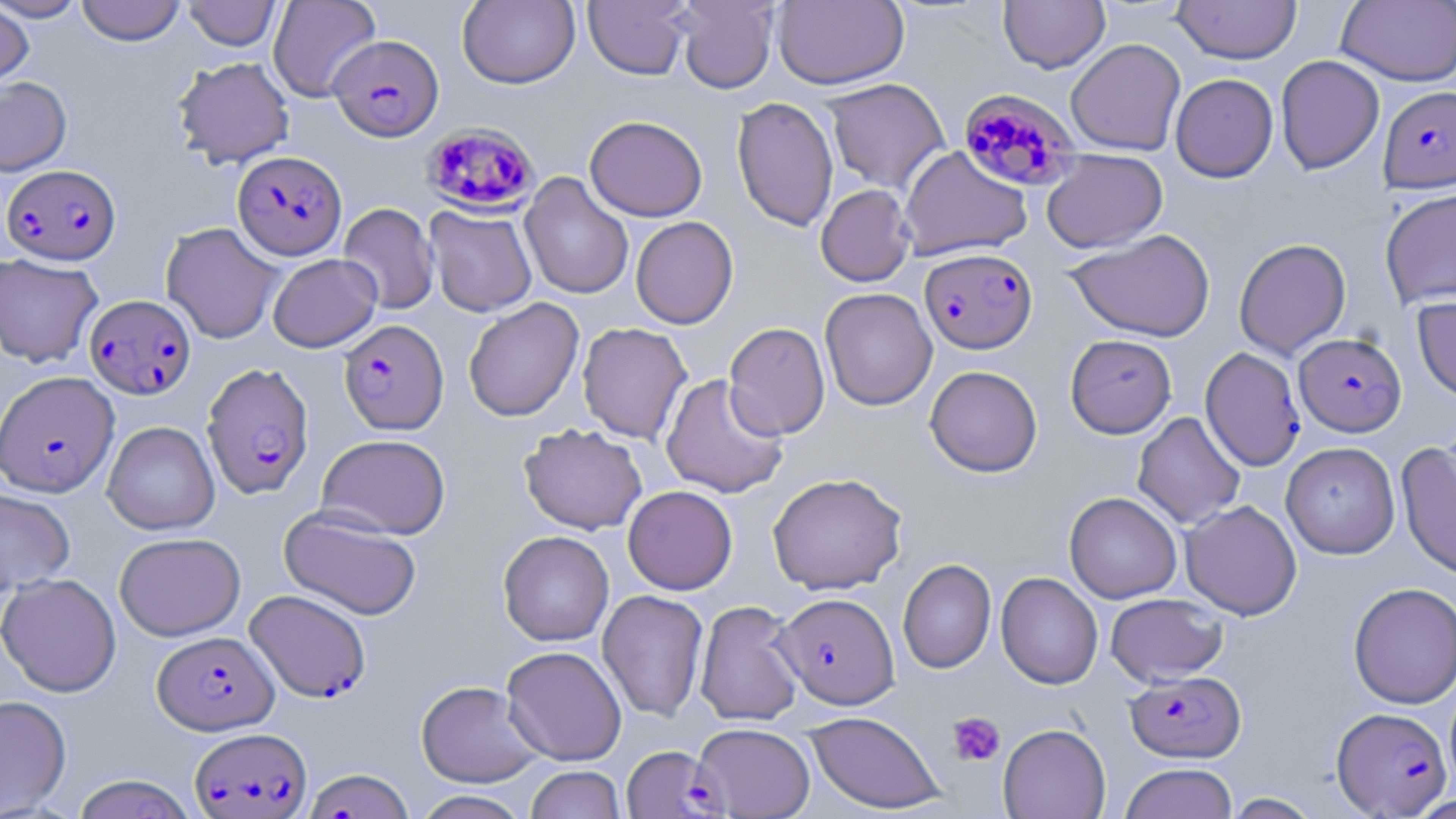

Approximate bounding boxes as [x1, y1, x2, y2] in pixels. Uninfected red blood cell locations (subset): [0, 0, 88, 21], [268, 0, 381, 101], [457, 0, 580, 89], [583, 0, 692, 80], [673, 0, 779, 94], [773, 0, 909, 89], [1337, 0, 1456, 87], [75, 1, 186, 46], [183, 1, 282, 50], [998, 1, 1110, 73], [1172, 1, 1302, 64], [0, 3, 34, 92], [1065, 38, 1186, 156], [1276, 55, 1384, 174], [171, 56, 295, 168], [1170, 73, 1279, 182], [0, 76, 72, 176], [822, 78, 950, 194], [732, 96, 839, 231], [585, 115, 708, 221], [899, 145, 1032, 261], [1041, 149, 1168, 253], [519, 172, 634, 300], [816, 185, 915, 286], [1379, 188, 1456, 309], [338, 203, 439, 315], [425, 206, 537, 317], [630, 216, 738, 329], [161, 222, 283, 344], [1066, 229, 1216, 342], [1234, 238, 1351, 360], [0, 252, 103, 368], [267, 253, 382, 352], [820, 287, 937, 411], [1412, 294, 1456, 401], [463, 298, 583, 422], [724, 321, 830, 440], [577, 322, 691, 444], [1065, 334, 1177, 439], [925, 365, 1042, 477], [660, 374, 789, 498], [1132, 412, 1245, 530], [102, 421, 219, 535], [518, 423, 647, 535], [316, 434, 451, 539], [1281, 441, 1400, 558], [1396, 442, 1456, 580], [767, 472, 907, 594], [623, 485, 737, 595], [0, 488, 75, 595], [1064, 492, 1182, 603], [1180, 500, 1302, 620], [280, 507, 422, 620], [497, 530, 614, 646], [114, 532, 245, 641], [898, 559, 996, 674], [996, 572, 1103, 689], [0, 573, 122, 697], [1348, 582, 1456, 709], [597, 590, 709, 722], [1105, 593, 1228, 686], [695, 600, 805, 727], [501, 645, 627, 765], [416, 680, 543, 787], [0, 695, 72, 816], [805, 711, 945, 814], [692, 723, 815, 818], [997, 723, 1111, 818], [1120, 763, 1238, 819], [525, 765, 626, 819], [71, 774, 198, 819], [412, 790, 532, 819], [1222, 792, 1324, 818]. Platelet locations: [947, 711, 1005, 766]. Plasmodium falciparum-infected red blood cell locations (subset): [328, 34, 444, 141], [1379, 86, 1456, 193], [957, 89, 1079, 192], [420, 121, 541, 216], [232, 150, 346, 260], [2, 164, 121, 265], [920, 247, 1037, 354], [85, 294, 196, 399], [339, 319, 448, 435], [1294, 333, 1406, 437], [1200, 347, 1306, 471], [202, 362, 315, 500], [0, 371, 119, 497], [245, 589, 371, 703], [775, 592, 899, 709], [152, 630, 279, 735], [1125, 669, 1246, 763], [1332, 706, 1452, 817], [190, 726, 311, 818], [622, 745, 723, 818]. Slide-level diagnosis: Plasmodium falciparum. Single field of view. May-Grünwald-Giemsa stain. Image is 1456×819 pixels. Thin blood film. Light microscopy. 1000x magnification.